Point out each Plasmodium parasite and classify it by life-cycle stage.
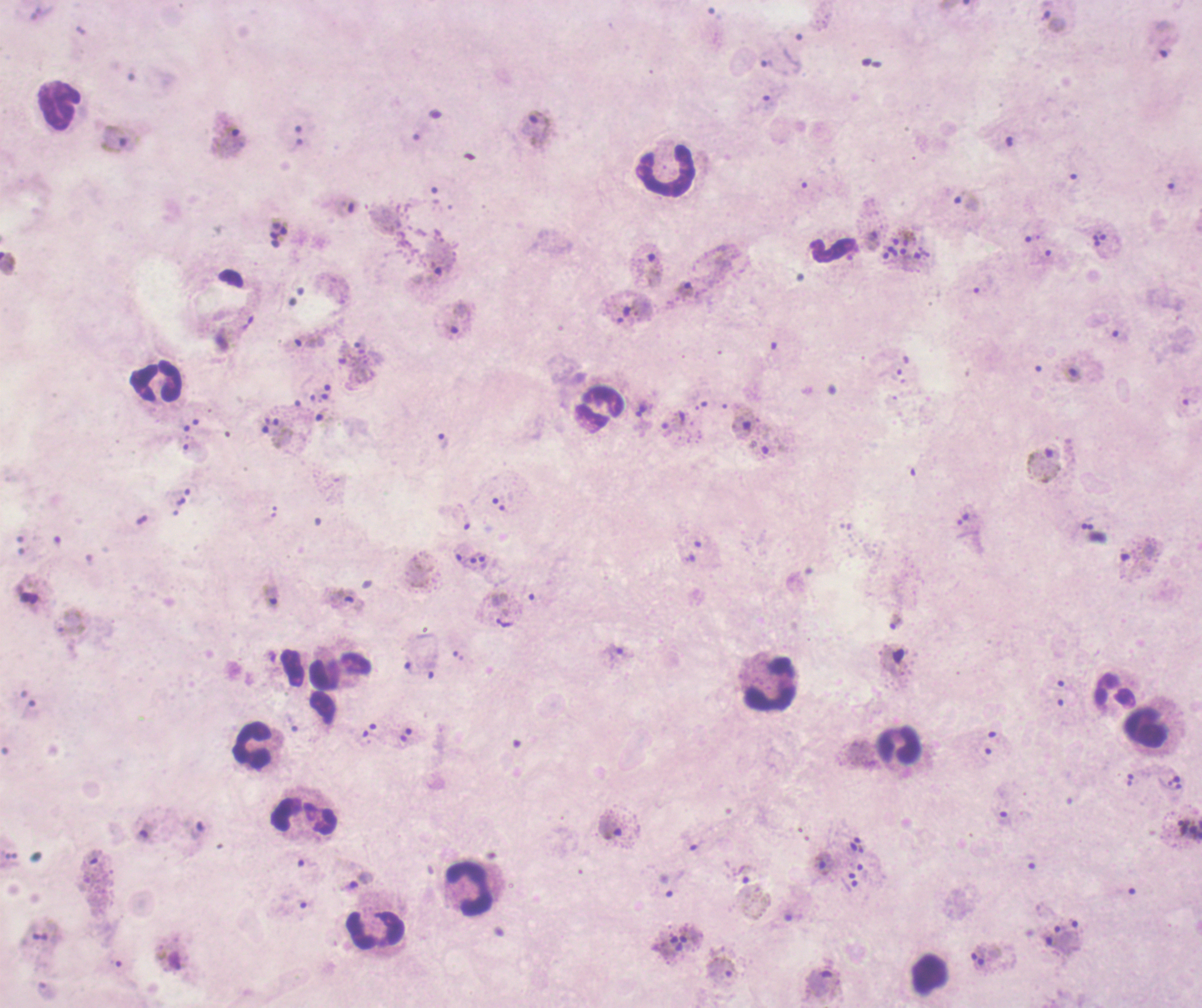
Approximate centers as {x, y} in pixels.
Trophozoites: {1054, 22}, {775, 67}, {537, 126}, {229, 138}, {118, 140}, {649, 265}, {686, 290}, {456, 320}, {309, 341}, {1072, 374}, {643, 410}, {674, 419}, {442, 440}, {1042, 465}, {270, 597}, {345, 601}, {504, 622}, {895, 623}, {617, 654}, {1004, 817}, {1183, 826}, {610, 827}, {823, 864}, {740, 874}, {361, 881}, {665, 886}, {691, 935}, {825, 982}.
Gametocytes: {894, 659}, {170, 960}.
No schizont forms observed.

Approximate centers as {x, y} in pixels.
Summary:
  - Leukocyte locations: {60, 106}, {666, 171}, {831, 251}, {156, 382}, {599, 409}, {771, 683}, {1115, 691}, {1146, 728}, {252, 745}, {899, 745}, {305, 817}, {469, 889}, {376, 929}, {929, 975}
  - Stain: Romanowsky
  - Preparation: thick smear of blood
  - Field of view: one from this slide
  - Image size: 1202×1008 pixels
  - Background quality: unsatisfactory
  - Magnification: 100x
  - Context: previously used in an actual diagnosis
  - Coloration quality: bad